Report the malaria status of this cell.
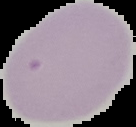
It is uninfected.

Summary:
  - Image type: segmented cell region on a black background
  - Image size: 136×127 pixels
  - Preparation: thin blood smear